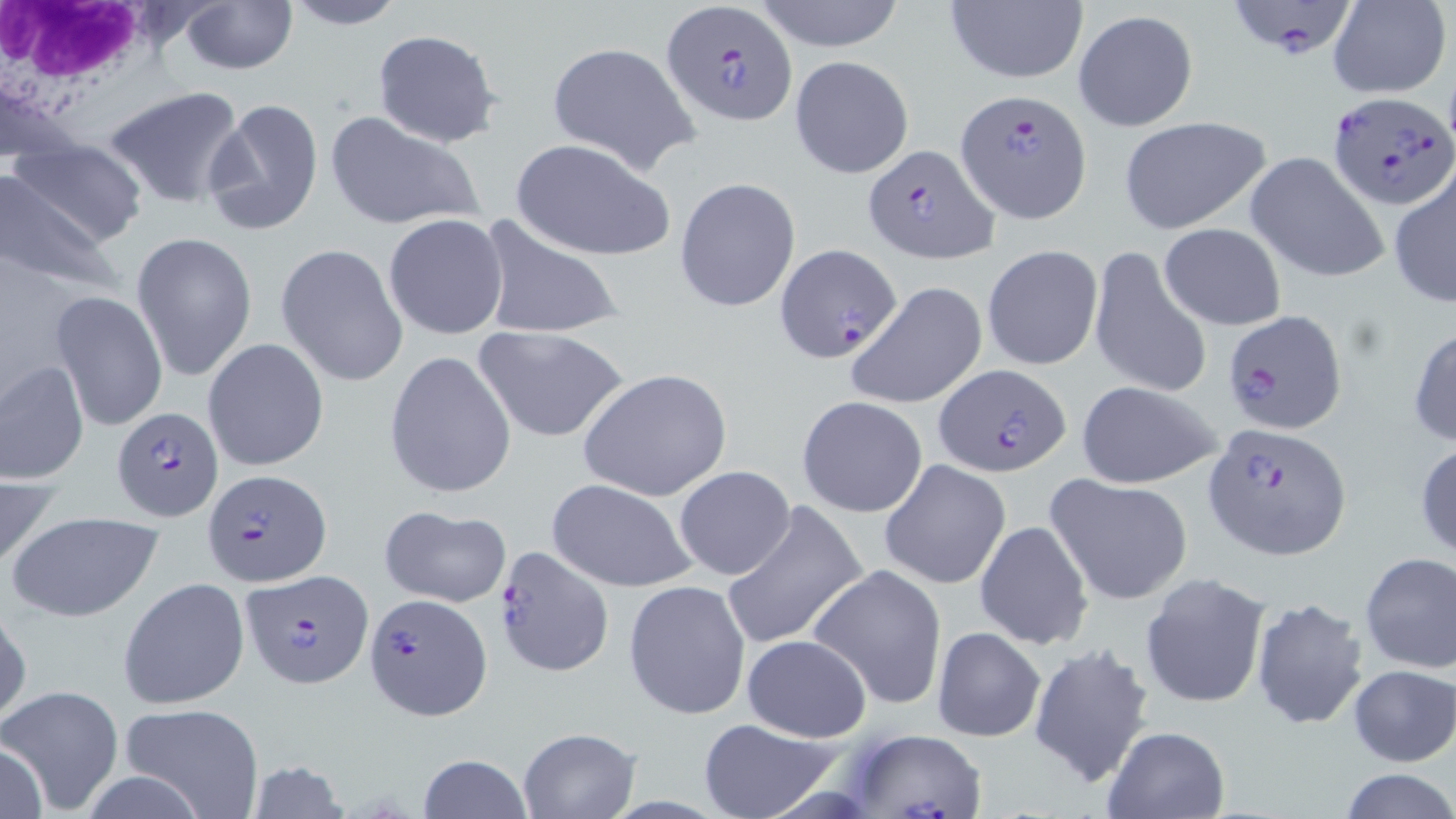

Approximate bounding boxes as (x1, y1, x2, y2) in pixels. White blood cell locations: (3, 1, 164, 121). Plasmodium falciparum-infected red blood cell locations: (1234, 0, 1353, 58), (661, 1, 796, 126), (1326, 91, 1456, 210), (957, 92, 1092, 223), (864, 144, 1000, 265), (775, 244, 902, 363), (1225, 309, 1349, 433), (937, 364, 1070, 474), (112, 406, 221, 520), (1204, 420, 1353, 560), (205, 469, 330, 587), (497, 545, 614, 676), (240, 568, 374, 686), (366, 593, 491, 719), (839, 729, 991, 819). Uninfected red blood cell locations: (179, 0, 297, 73), (281, 0, 408, 29), (748, 0, 911, 51), (943, 0, 1087, 86), (1329, 1, 1451, 97), (1073, 10, 1199, 131), (373, 29, 504, 149), (546, 40, 701, 175), (789, 55, 914, 179), (102, 86, 248, 209), (203, 97, 324, 236), (324, 109, 485, 234), (1117, 116, 1272, 235), (510, 137, 675, 262), (6, 140, 147, 256), (1246, 152, 1389, 283), (1387, 166, 1455, 309), (0, 174, 122, 294), (674, 177, 800, 311), (383, 213, 509, 340), (475, 214, 627, 343), (1159, 223, 1287, 330), (132, 231, 257, 380), (276, 244, 408, 387), (981, 244, 1103, 371), (1089, 246, 1213, 401), (846, 280, 989, 410), (51, 290, 168, 432), (472, 324, 629, 443), (1407, 325, 1456, 447), (203, 338, 329, 472), (384, 350, 516, 498), (0, 359, 89, 485), (577, 367, 734, 504), (1075, 381, 1224, 489), (797, 395, 929, 518), (1414, 440, 1456, 563), (880, 460, 1011, 589), (673, 466, 797, 580), (0, 471, 58, 577), (1046, 475, 1192, 605), (546, 479, 699, 593), (721, 500, 869, 653), (378, 504, 512, 607), (6, 510, 165, 622), (974, 520, 1092, 651), (1358, 550, 1455, 674), (808, 563, 948, 711), (1139, 575, 1269, 709), (118, 578, 246, 708), (624, 579, 750, 719), (1250, 598, 1370, 729), (0, 600, 30, 729), (932, 627, 1045, 743), (742, 634, 872, 743), (1027, 642, 1156, 788), (1348, 664, 1456, 767), (0, 685, 124, 811), (118, 703, 264, 819), (695, 717, 845, 819), (1099, 725, 1232, 819), (517, 728, 640, 818), (0, 737, 49, 819), (416, 753, 534, 819), (244, 761, 350, 819), (1338, 768, 1456, 819). Slide-level diagnosis: Plasmodium falciparum. Optical microscopy. Thin blood film. 1000x magnification. May-Grünwald-Giemsa stain. Image is 1456×819 pixels. Single field of view.